State the preparation type.
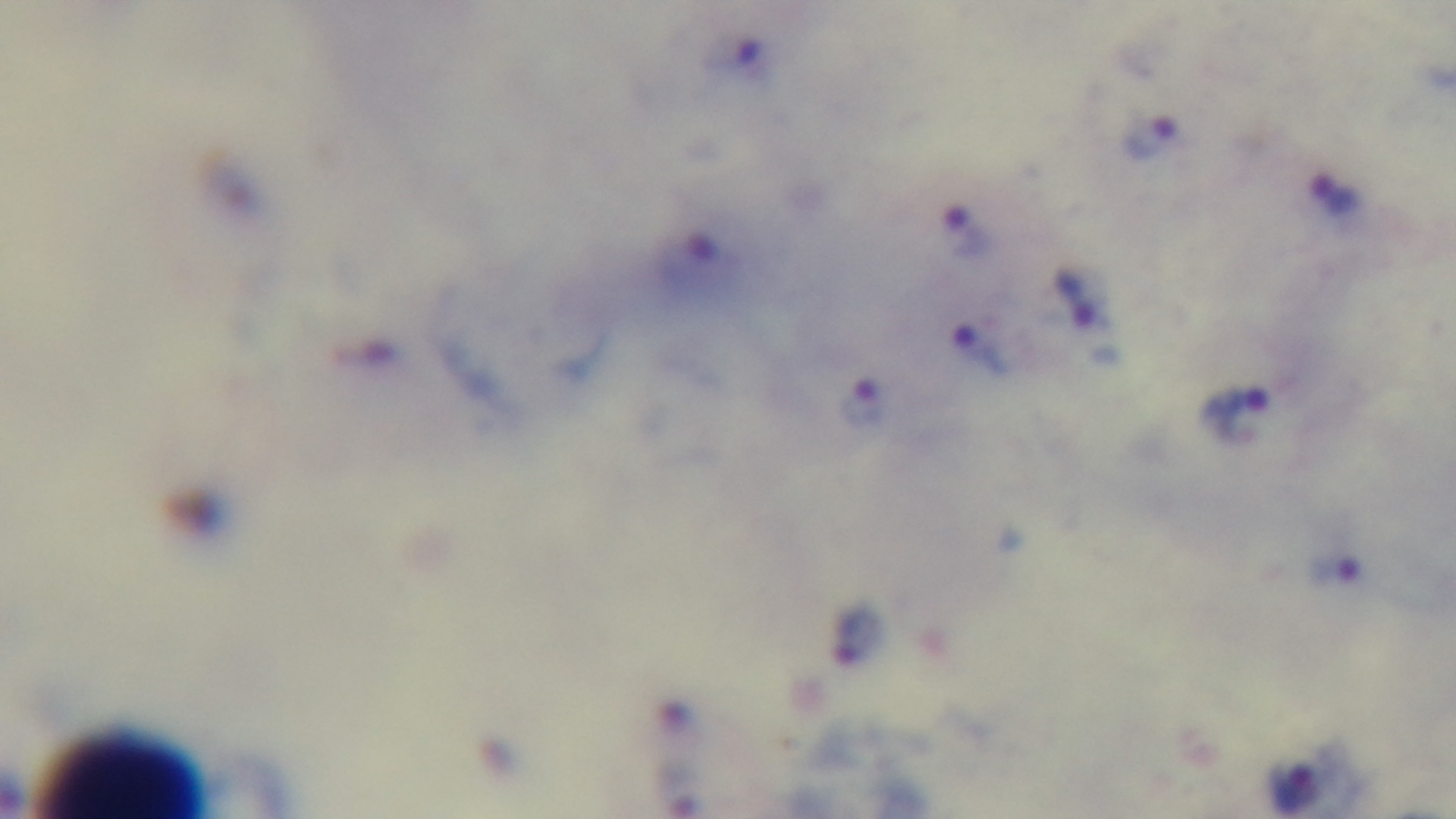
A thick smear.

field of view = single
objective = 100x oil immersion
capture = mounted 4K digital camera
stain = Giemsa
modality = light microscopy
malaria status = positive